Point out each Plasmodium parasite.
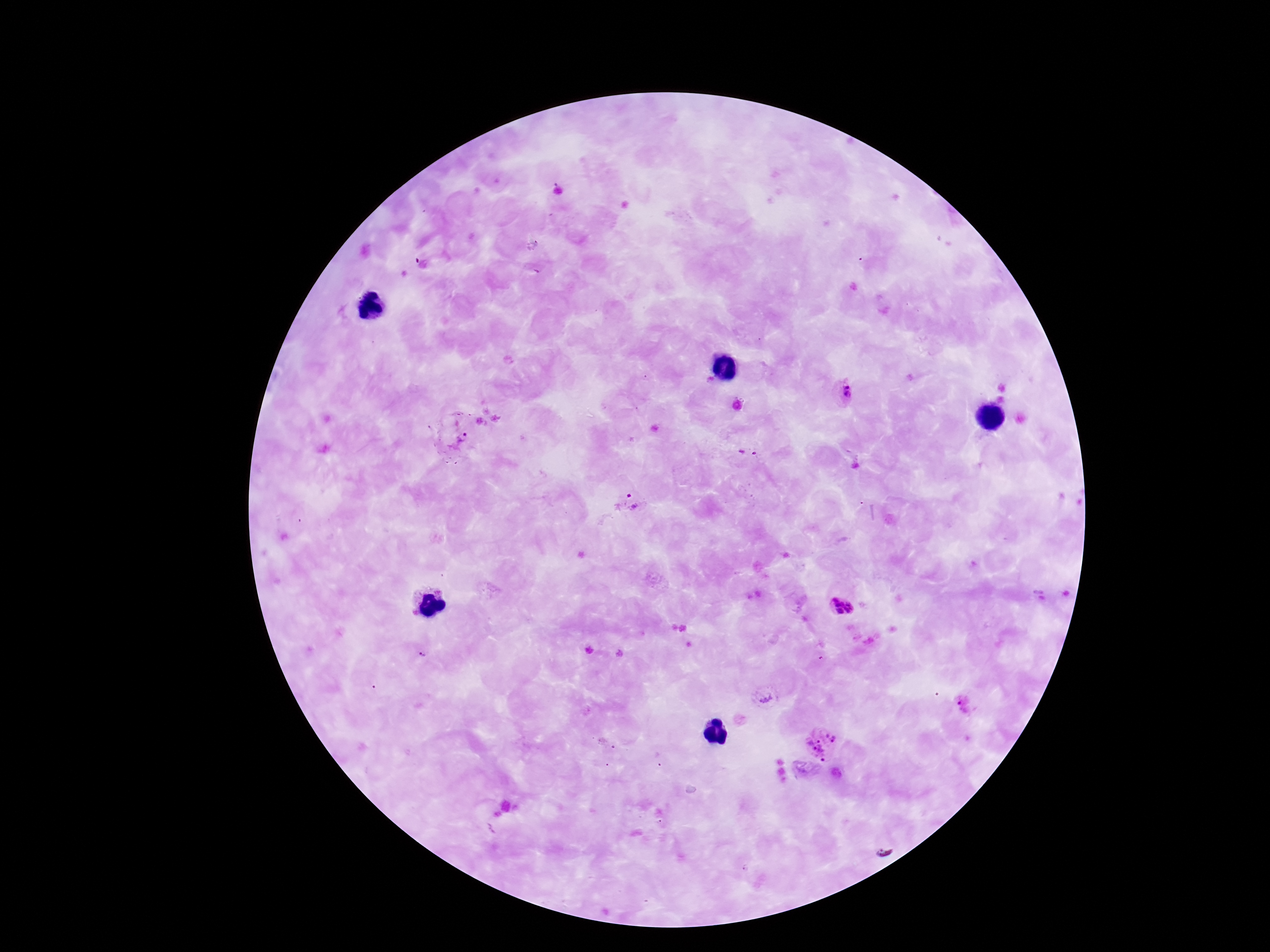
Approximate centers as (x, y) in pixels.
Plasmodium parasites: (844, 391), (456, 434), (634, 502), (840, 607), (423, 655), (765, 697), (965, 705), (820, 743).

{
  "capture": "smartphone camera through the microscope eyepiece",
  "field_of_view": "single",
  "image_size": "1270×952 pixels",
  "patient_malaria_status": "infected",
  "magnification": "100x",
  "preparation": "thick blood film",
  "stain": "Giemsa"
}